Describe the morphology of the erythrocytes.
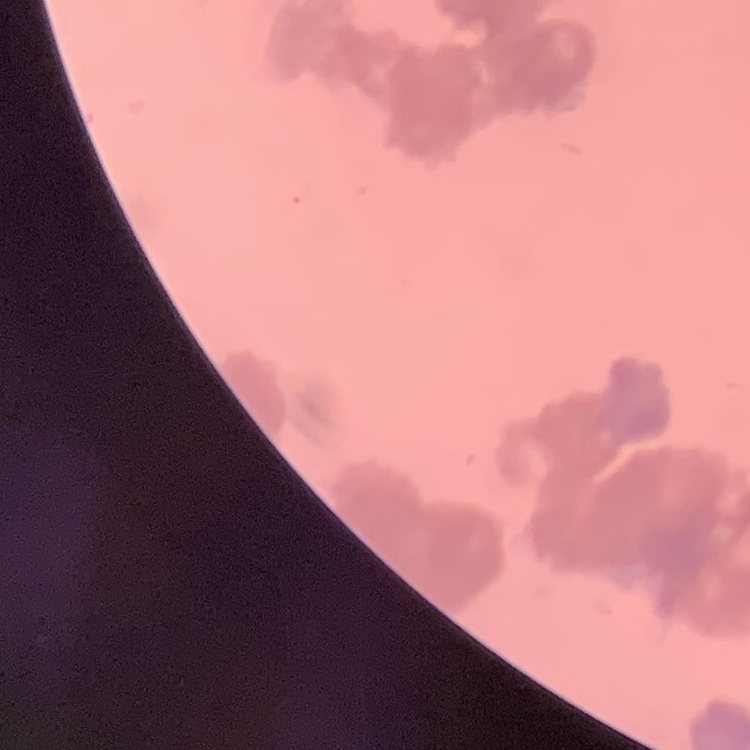

They show rouleaux formation.

Summary:
  - Image type: one tile cut from a larger photomicrograph
  - Stain: Field's or Giemsa
  - Preparation: thin peripheral smear